Name the cell type shown.
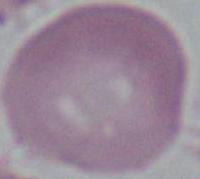

This is an erythrocyte.

Summary:
  - Modality: photomicrograph
  - Magnification: 1000x